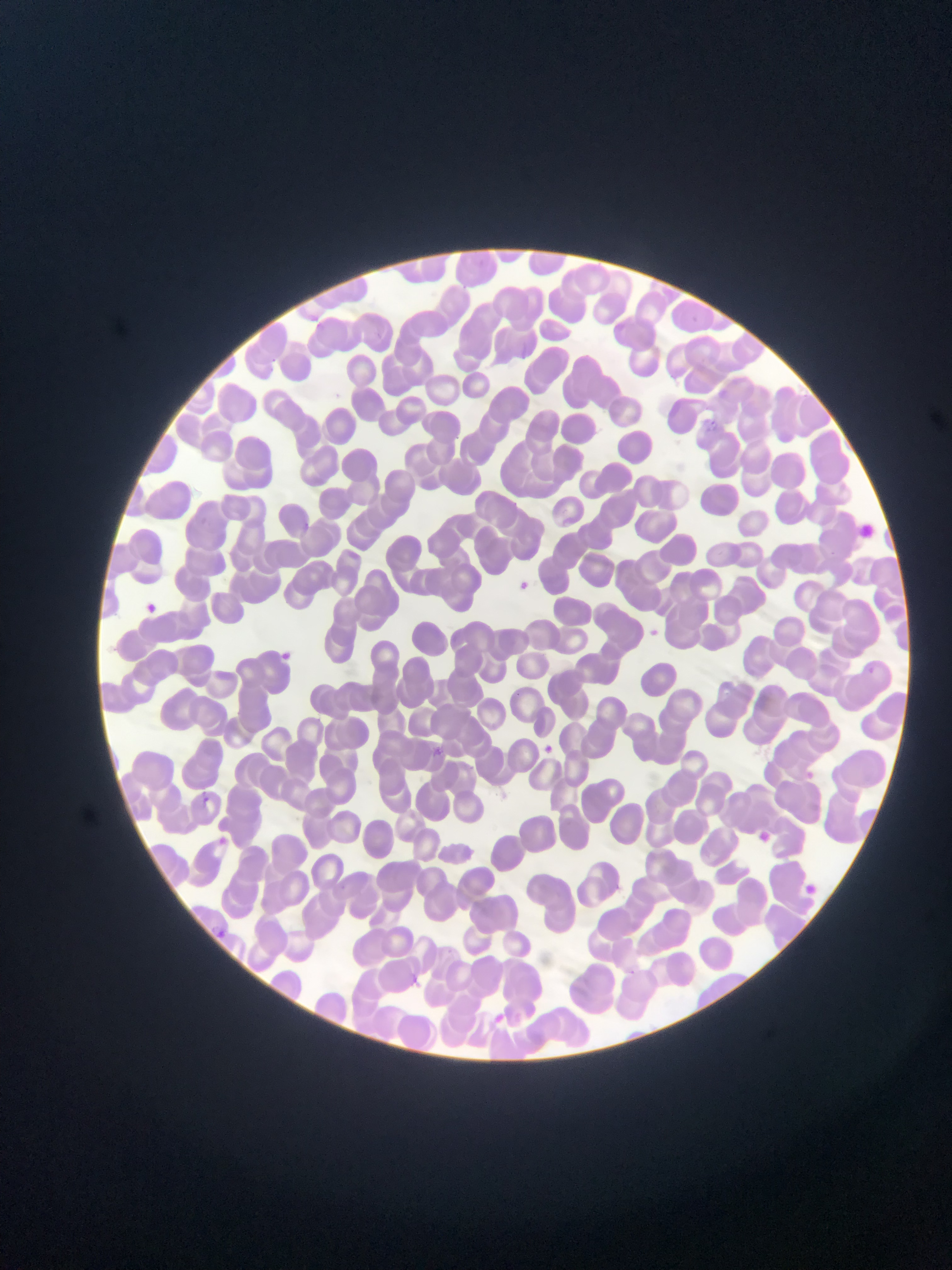

{
  "field_of_view": "single",
  "capture": "mobile-phone photograph through a microscope",
  "image_size": "952×1270 pixels",
  "malaria_parasite_locations": "approximate bounding boxes as (left, top, right, bottom) in pixels: (458, 285, 471, 291), (692, 313, 711, 331), (308, 317, 325, 334), (371, 331, 385, 343), (272, 354, 278, 374), (800, 387, 810, 403), (706, 417, 720, 430), (303, 523, 312, 535), (827, 549, 839, 561), (509, 574, 543, 593), (146, 604, 161, 613), (643, 626, 665, 641), (280, 647, 298, 664), (865, 663, 875, 677), (538, 739, 554, 758), (427, 741, 448, 766), (801, 767, 815, 785), (200, 789, 212, 806), (219, 834, 233, 846), (611, 879, 625, 897), (340, 884, 353, 896), (210, 928, 229, 942), (410, 969, 427, 985), (484, 1012, 507, 1023)",
  "preparation": "thin blood film",
  "country": "Ghana"
}